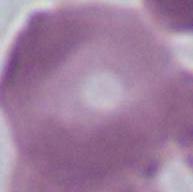
Summary:
  - Modality: photomicrograph
  - Magnification: 1000x
  - Identification: erythrocyte